Classify this cell by malaria status.
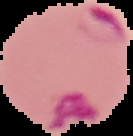

It is parasitized.

image size = 133×136 pixels
preparation = thin blood film
image type = segmented cell region on a black background